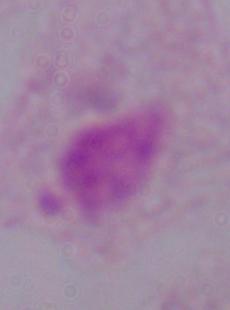
A trichomonad is shown. 1000x magnification. Photomicrograph.